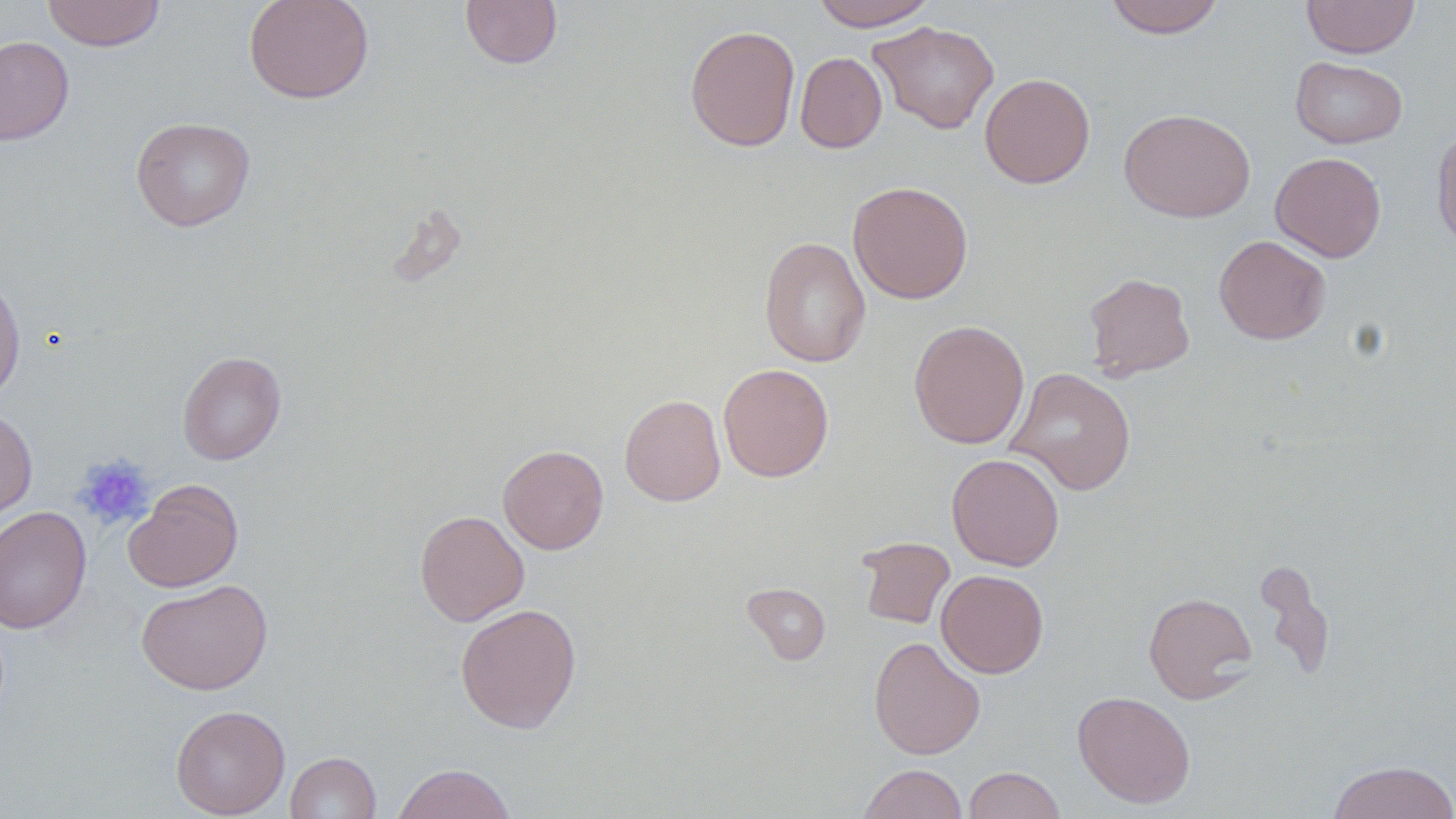

Approximate bounding boxes as (x1,y1)-(x2,y2) corner pairs in pixels. Platelet locations: (73,454)-(154,529). Uninfected red blood cell locations: (42,0)-(165,51), (243,0)-(375,104), (460,0)-(562,69), (810,0)-(938,31), (1103,0)-(1225,38), (1301,0)-(1419,58), (868,20)-(999,134), (684,24)-(800,152), (0,36)-(74,146), (795,52)-(887,153), (1290,56)-(1408,149), (979,72)-(1095,188), (1119,107)-(1256,223), (131,117)-(255,231), (1432,125)-(1456,254), (1270,152)-(1386,262), (847,181)-(973,305), (1214,235)-(1331,344), (759,236)-(871,368), (1083,272)-(1196,381), (0,273)-(26,405), (908,319)-(1030,449), (177,351)-(286,465), (718,363)-(834,482), (1006,367)-(1137,496), (619,394)-(726,506), (0,406)-(37,521), (498,444)-(609,554), (946,452)-(1065,571), (124,479)-(243,592), (0,506)-(91,634), (414,509)-(529,626), (856,536)-(955,629), (1255,559)-(1335,680), (936,569)-(1049,678), (136,578)-(273,695), (741,582)-(831,665), (1143,592)-(1257,703), (455,603)-(582,733), (868,636)-(985,760), (1072,690)-(1196,808), (170,705)-(290,818), (285,751)-(381,819), (1326,760)-(1456,819), (392,763)-(517,819), (858,763)-(967,819), (963,766)-(1066,818). Slide-level diagnosis: no evidence of blood parasites. Optical microscopy. 1000x magnification. Single field of view. Thin blood smear. Image is 1456×819 pixels. May-Grünwald-Giemsa stain.